Identify the parasite.
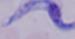
This is a trypanosome.

modality = photomicrograph
magnification = 1000x